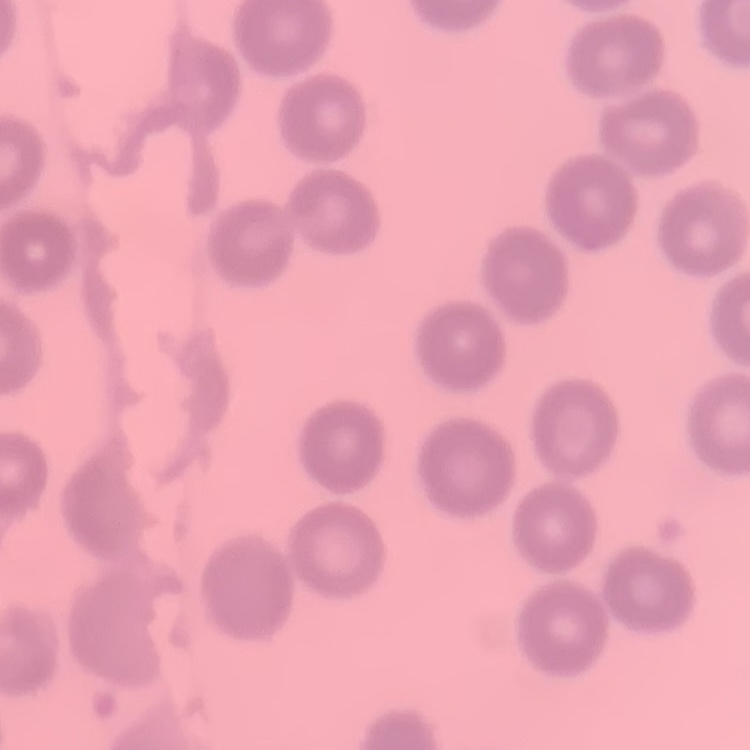
The erythrocytes show no rouleaux formation. Thin blood film. Stained with either Field's or Giemsa. Square crop of a larger photomicrograph.